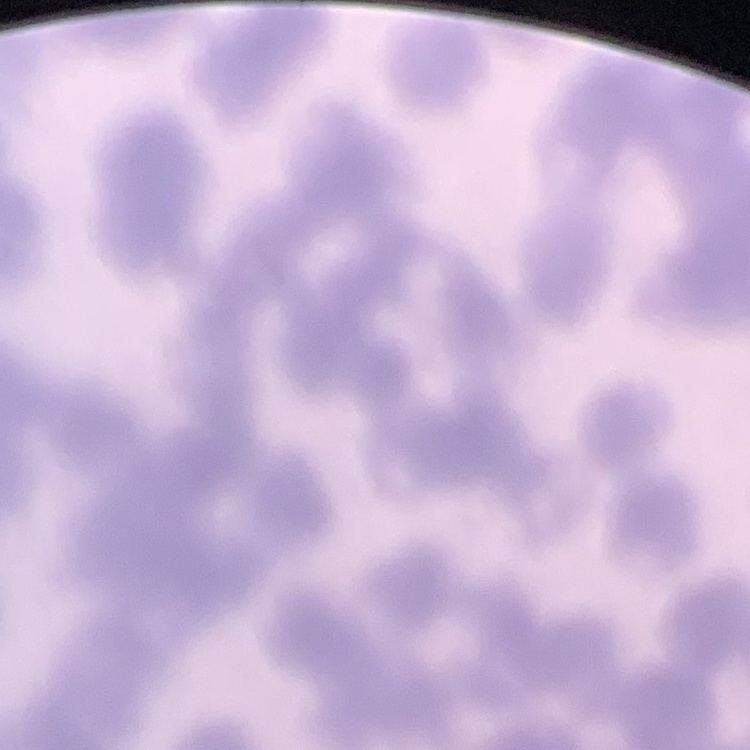
red blood cell morphology = rouleaux formation
stain = Field's or Giemsa
preparation = thin blood smear
image type = one tile cut from a larger photomicrograph